Locate every Plasmodium falciparum-infected red blood cell.
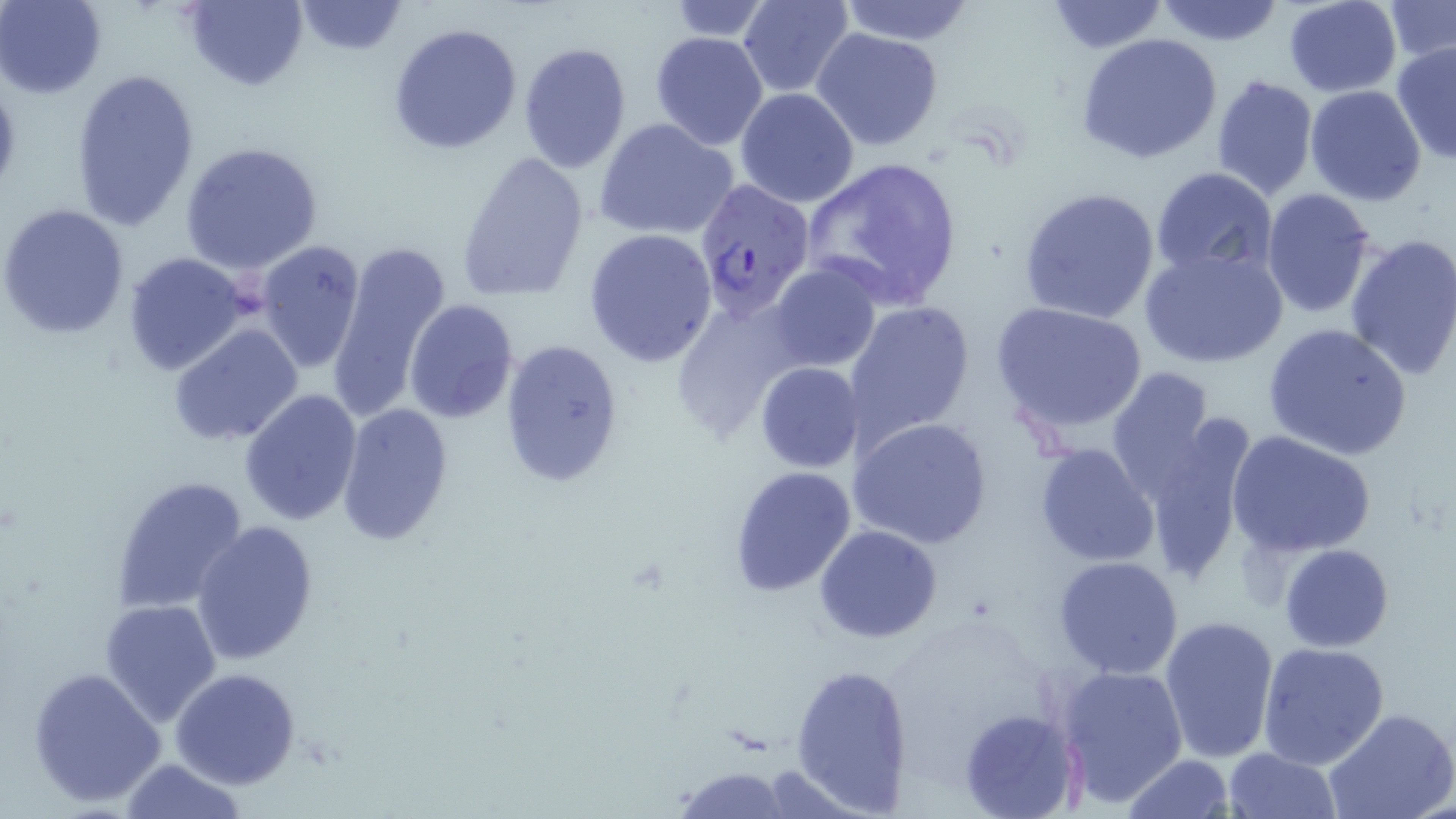
Approximate bounding boxes as named x1/y1/x2/y2 corners in pixels.
Plasmodium falciparum-infected red blood cells: (x1=692, y1=178, x2=814, y2=317).

slide-level diagnosis = Plasmodium falciparum
preparation = thin blood smear
modality = optical microscopy
stain = May-Grünwald-Giemsa
field of view = one of a larger specimen
uninfected red blood cell locations = approximate bounding boxes as named x1/y1/x2/y2 corners in pixels: (x1=1, y1=0, x2=106, y2=97), (x1=185, y1=0, x2=309, y2=90), (x1=737, y1=0, x2=855, y2=99), (x1=837, y1=0, x2=978, y2=46), (x1=1155, y1=0, x2=1284, y2=46), (x1=1282, y1=0, x2=1401, y2=97), (x1=1386, y1=0, x2=1456, y2=64), (x1=291, y1=1, x2=408, y2=55), (x1=664, y1=1, x2=772, y2=41), (x1=1043, y1=1, x2=1168, y2=53), (x1=388, y1=22, x2=523, y2=155), (x1=811, y1=28, x2=946, y2=152), (x1=649, y1=32, x2=771, y2=150), (x1=1077, y1=32, x2=1224, y2=164), (x1=517, y1=41, x2=632, y2=173), (x1=1391, y1=43, x2=1456, y2=164), (x1=69, y1=68, x2=199, y2=232), (x1=1210, y1=74, x2=1319, y2=202), (x1=1305, y1=85, x2=1428, y2=206), (x1=735, y1=87, x2=858, y2=208), (x1=595, y1=117, x2=738, y2=241), (x1=179, y1=140, x2=325, y2=274), (x1=455, y1=148, x2=591, y2=303), (x1=800, y1=156, x2=965, y2=313), (x1=1150, y1=167, x2=1277, y2=278), (x1=1020, y1=187, x2=1162, y2=325), (x1=1259, y1=188, x2=1378, y2=317), (x1=1, y1=202, x2=130, y2=339), (x1=584, y1=226, x2=718, y2=367), (x1=1343, y1=233, x2=1456, y2=382), (x1=327, y1=237, x2=452, y2=418), (x1=254, y1=241, x2=367, y2=373), (x1=1140, y1=245, x2=1287, y2=370), (x1=122, y1=252, x2=251, y2=375), (x1=768, y1=263, x2=880, y2=371), (x1=668, y1=292, x2=809, y2=439), (x1=403, y1=300, x2=519, y2=422), (x1=842, y1=300, x2=977, y2=446), (x1=989, y1=300, x2=1148, y2=436), (x1=168, y1=322, x2=304, y2=446), (x1=1262, y1=324, x2=1411, y2=461), (x1=500, y1=337, x2=625, y2=487), (x1=756, y1=363, x2=863, y2=472), (x1=1105, y1=367, x2=1220, y2=507), (x1=240, y1=389, x2=363, y2=526), (x1=335, y1=402, x2=454, y2=546), (x1=1136, y1=414, x2=1255, y2=585), (x1=848, y1=417, x2=993, y2=550), (x1=1226, y1=430, x2=1375, y2=558), (x1=1034, y1=443, x2=1162, y2=567), (x1=728, y1=466, x2=856, y2=595), (x1=111, y1=475, x2=250, y2=616), (x1=189, y1=521, x2=320, y2=665), (x1=815, y1=524, x2=942, y2=644), (x1=1279, y1=543, x2=1394, y2=651), (x1=1053, y1=556, x2=1183, y2=679), (x1=100, y1=599, x2=222, y2=726), (x1=1160, y1=615, x2=1281, y2=765), (x1=1258, y1=641, x2=1390, y2=769), (x1=790, y1=663, x2=915, y2=813), (x1=1054, y1=663, x2=1189, y2=808), (x1=28, y1=666, x2=168, y2=808), (x1=171, y1=668, x2=300, y2=789), (x1=959, y1=707, x2=1082, y2=819), (x1=1325, y1=710, x2=1456, y2=819), (x1=1222, y1=746, x2=1342, y2=818), (x1=1123, y1=755, x2=1234, y2=818), (x1=120, y1=757, x2=246, y2=819), (x1=668, y1=765, x2=798, y2=819)
magnification = 1000x
image size = 1456×819 pixels